Assess this cell for malaria.
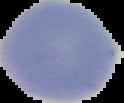
Uninfected.

Summary:
  - Image type: segmented cell region on a black background
  - Image size: 124×103 pixels
  - Preparation: thin blood smear